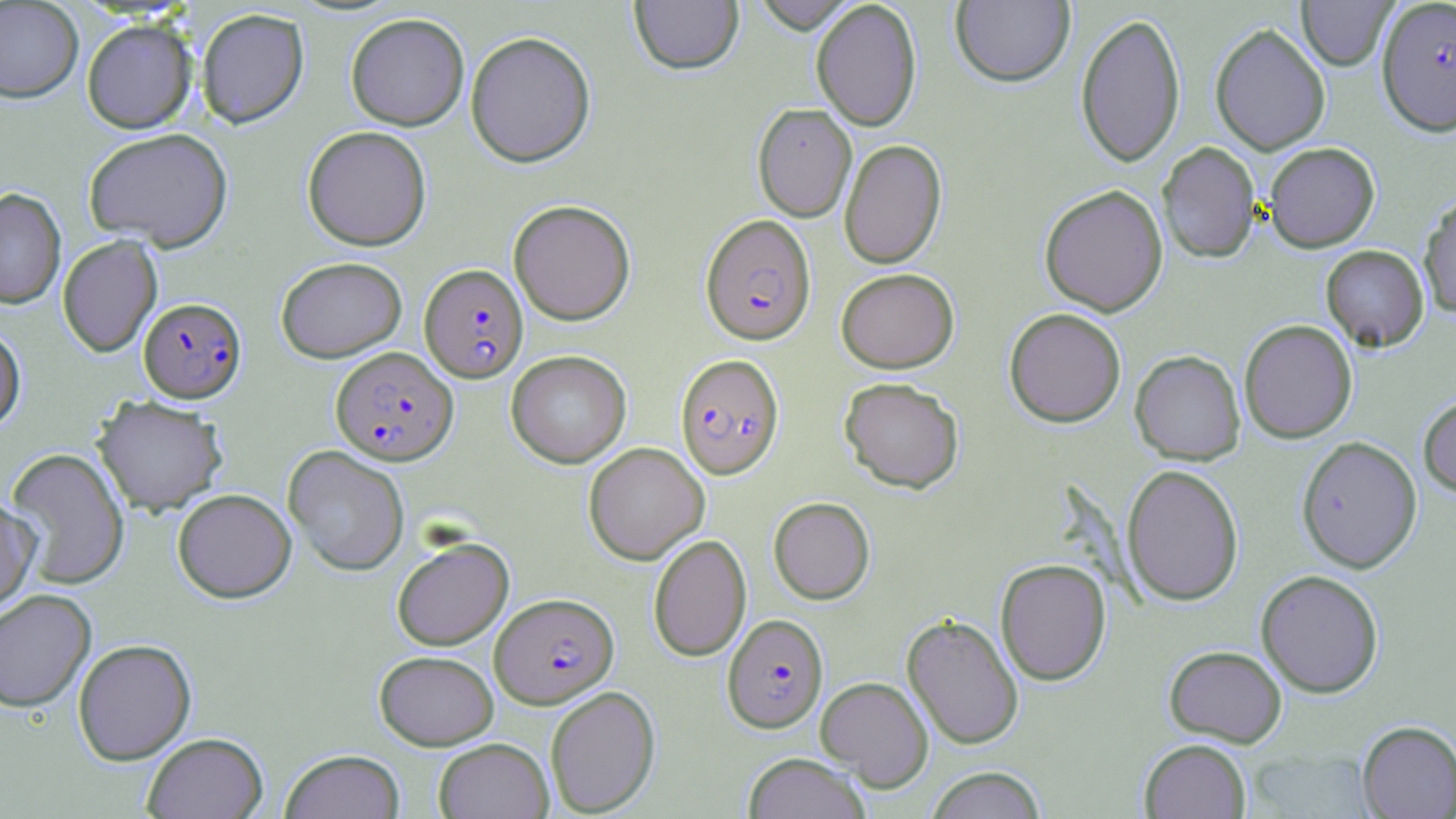 Approximate bounding boxes as [x1, y1, x2, y2] in pixels. Uninfected red blood cell locations: [750, 0, 860, 33], [0, 1, 83, 103], [629, 1, 744, 75], [810, 1, 922, 131], [950, 1, 1074, 87], [1296, 1, 1397, 71], [196, 8, 309, 129], [1075, 11, 1186, 168], [345, 12, 470, 130], [81, 19, 197, 133], [1209, 22, 1331, 155], [465, 30, 596, 167], [752, 103, 857, 221], [302, 125, 431, 251], [83, 127, 233, 251], [839, 139, 947, 269], [1157, 142, 1260, 263], [1264, 142, 1380, 252], [1039, 184, 1169, 316], [0, 187, 66, 309], [1418, 194, 1456, 319], [508, 199, 636, 325], [57, 235, 163, 358], [1321, 244, 1429, 352], [275, 256, 407, 363], [836, 268, 959, 373], [1004, 308, 1127, 427], [1239, 319, 1358, 443], [0, 326, 26, 433], [506, 350, 631, 468], [1130, 350, 1245, 465], [839, 377, 965, 493], [92, 394, 228, 516], [1418, 394, 1456, 499], [1297, 436, 1422, 573], [583, 442, 709, 565], [283, 445, 409, 577], [5, 447, 130, 589], [1121, 464, 1244, 606], [172, 488, 297, 603], [0, 494, 40, 614], [768, 496, 875, 604], [648, 533, 751, 661], [391, 537, 513, 650], [995, 558, 1111, 685], [1256, 569, 1384, 697], [0, 589, 96, 713], [902, 613, 1024, 750], [72, 639, 196, 765], [1164, 644, 1287, 747], [374, 650, 498, 750], [816, 676, 934, 791], [544, 685, 661, 816], [1357, 720, 1456, 818], [142, 732, 268, 819], [434, 737, 553, 818], [1139, 739, 1251, 818], [280, 749, 405, 819], [742, 752, 871, 819], [924, 766, 1046, 818]. Plasmodium falciparum-infected red blood cell locations: [1377, 0, 1456, 136], [700, 214, 816, 345], [419, 264, 529, 383], [139, 297, 246, 402], [331, 346, 458, 466], [675, 353, 785, 479], [490, 592, 618, 708], [723, 614, 828, 732]. Slide-level diagnosis: Plasmodium falciparum. One field of a larger specimen. Captured at 1000x magnification. Optical microscopy. Thin blood smear. May-Grünwald-Giemsa stain. Image is 1456×819 pixels.